Locate every blood parasite and identify its species.
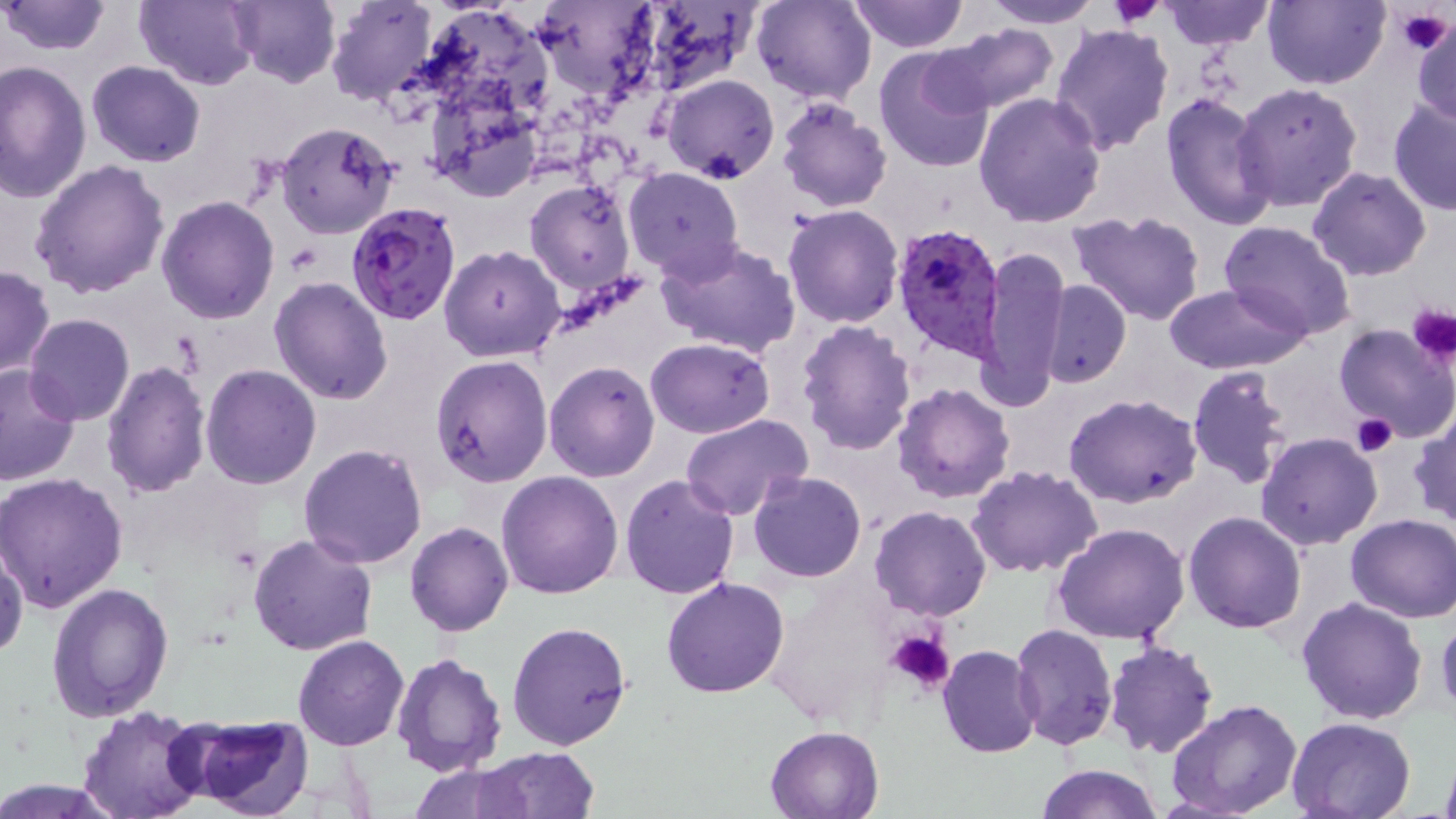

Approximate bounding boxes as (x1, y1, x2, y2) in pixels.
Plasmodium falciparum-infected red blood cells: (347, 202, 462, 324), (892, 223, 1005, 362).
No Plasmodium ovale, Plasmodium malariae, Plasmodium vivax, Babesia divergens, or Trypanosoma brucei observed.

Uninfected red blood cell locations: (2, 0, 112, 55), (227, 0, 342, 89), (326, 0, 438, 106), (414, 0, 555, 125), (751, 0, 875, 104), (985, 0, 1101, 27), (1161, 0, 1274, 49), (1262, 0, 1389, 89), (133, 1, 258, 88), (849, 1, 967, 51), (534, 2, 659, 101), (631, 2, 762, 94), (1409, 14, 1455, 128), (934, 22, 1058, 115), (1051, 22, 1175, 156), (873, 46, 996, 174), (0, 60, 92, 202), (87, 61, 205, 168), (663, 74, 779, 184), (1233, 82, 1363, 212), (426, 92, 543, 202), (974, 92, 1106, 229), (1161, 92, 1277, 231), (1388, 95, 1455, 217), (775, 99, 893, 213), (276, 121, 398, 239), (29, 160, 170, 300), (1308, 166, 1431, 281), (623, 167, 743, 278), (524, 179, 635, 296), (155, 195, 280, 323), (643, 196, 769, 326), (783, 205, 904, 328), (1068, 210, 1209, 327), (1218, 220, 1358, 340), (655, 237, 801, 361), (440, 246, 566, 363), (979, 248, 1068, 405), (0, 266, 53, 379), (269, 276, 394, 404), (1040, 279, 1131, 389), (1162, 284, 1308, 375), (25, 313, 134, 425), (796, 319, 917, 454), (1333, 321, 1455, 444), (646, 337, 774, 437), (430, 354, 554, 487), (543, 360, 661, 481), (100, 362, 211, 501), (0, 364, 81, 485), (202, 364, 322, 488), (1185, 366, 1296, 490), (893, 382, 1015, 502), (1063, 393, 1205, 509), (1410, 410, 1456, 528), (681, 415, 811, 522), (1255, 432, 1382, 550), (299, 443, 428, 569), (967, 465, 1103, 578), (497, 471, 624, 598), (749, 471, 867, 583), (0, 472, 129, 612), (619, 474, 740, 600), (1018, 482, 1186, 614), (870, 505, 993, 621), (1185, 511, 1306, 632), (1345, 513, 1456, 624), (406, 521, 514, 636), (1051, 524, 1191, 645), (247, 534, 377, 657), (1, 543, 27, 659), (661, 577, 789, 698), (47, 583, 175, 722), (1296, 596, 1428, 723), (1436, 610, 1456, 723), (507, 622, 633, 751), (1009, 625, 1119, 750), (293, 635, 410, 751), (1101, 639, 1219, 758), (938, 645, 1043, 759), (390, 651, 506, 778), (1165, 699, 1303, 819), (79, 705, 207, 819), (182, 715, 313, 818), (1286, 716, 1417, 819), (765, 725, 882, 818), (477, 747, 600, 818), (1438, 748, 1456, 819), (408, 763, 537, 819), (1034, 763, 1164, 819). Platelet locations: (1111, 0, 1166, 29), (1394, 6, 1454, 55), (1407, 305, 1456, 365), (1351, 413, 1398, 456), (884, 629, 955, 694). Slide-level diagnosis: Plasmodium falciparum. One field of a larger specimen. May-Grünwald-Giemsa stain. Image is 1456×819 pixels. Thin blood smear. Light microscopy. 1000x magnification.